Locate every blood parasite and identify its species.
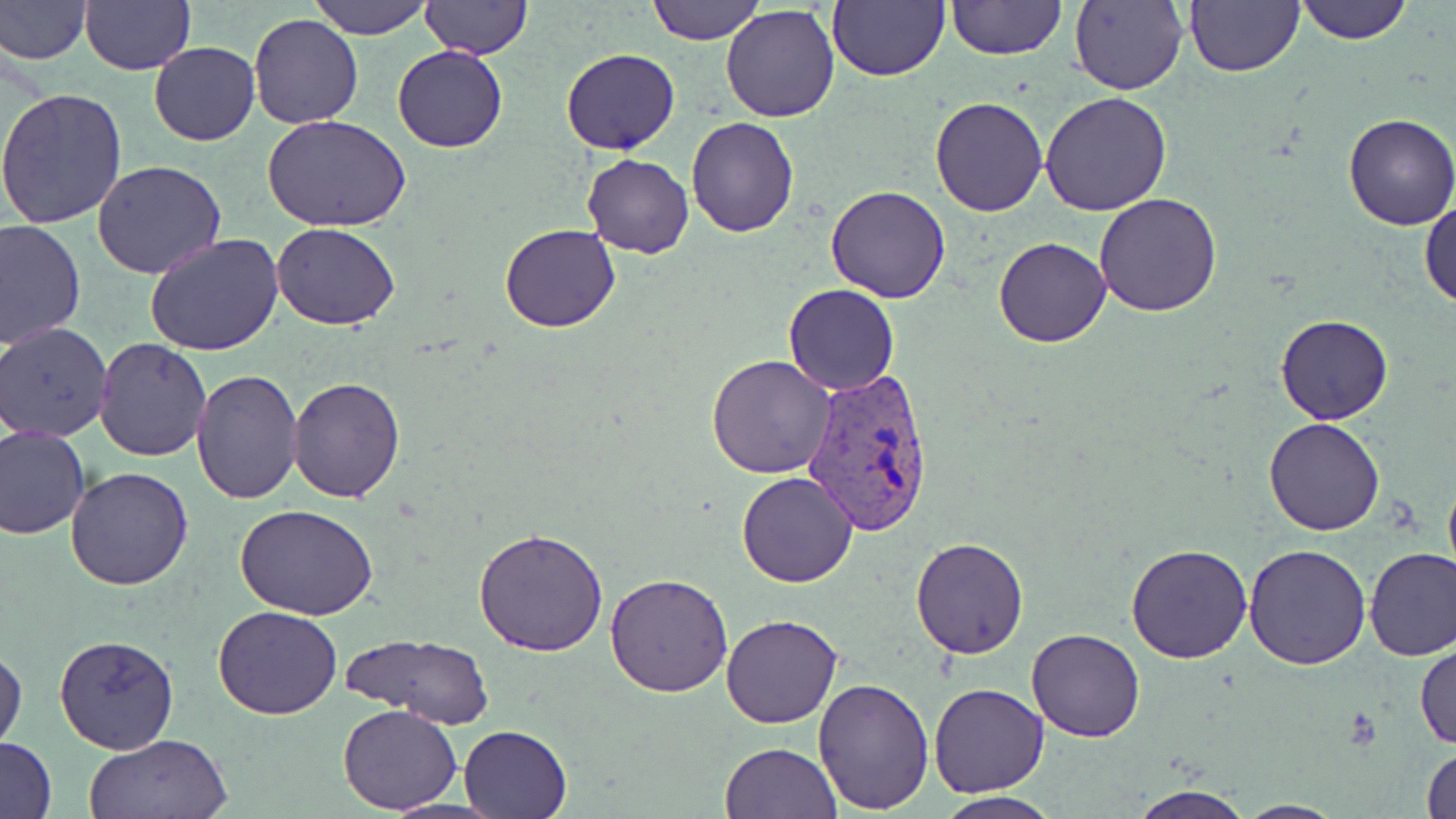

Approximate bounding boxes as named x1/y1/x2/y2 corners in pixels.
Plasmodium vivax-infected red blood cells: (x1=798, y1=365, x2=938, y2=537).
No Plasmodium falciparum, Plasmodium ovale, Plasmodium malariae, Babesia divergens, or Trypanosoma brucei observed.

Summary:
  - Uninfected red blood cell locations: (x1=0, y1=0, x2=91, y2=66), (x1=80, y1=0, x2=195, y2=75), (x1=309, y1=0, x2=433, y2=40), (x1=422, y1=0, x2=529, y2=59), (x1=647, y1=0, x2=763, y2=44), (x1=826, y1=0, x2=948, y2=83), (x1=947, y1=0, x2=1065, y2=61), (x1=1184, y1=0, x2=1305, y2=76), (x1=1294, y1=0, x2=1415, y2=45), (x1=1069, y1=1, x2=1187, y2=94), (x1=720, y1=3, x2=840, y2=123), (x1=250, y1=13, x2=363, y2=129), (x1=148, y1=41, x2=261, y2=146), (x1=392, y1=44, x2=507, y2=153), (x1=560, y1=48, x2=679, y2=156), (x1=0, y1=89, x2=129, y2=231), (x1=1040, y1=92, x2=1172, y2=214), (x1=930, y1=97, x2=1048, y2=217), (x1=1342, y1=111, x2=1456, y2=231), (x1=263, y1=114, x2=410, y2=234), (x1=685, y1=118, x2=800, y2=237), (x1=581, y1=152, x2=694, y2=258), (x1=92, y1=162, x2=226, y2=281), (x1=825, y1=184, x2=951, y2=303), (x1=1094, y1=193, x2=1222, y2=318), (x1=1420, y1=197, x2=1456, y2=310), (x1=0, y1=218, x2=86, y2=349), (x1=272, y1=223, x2=401, y2=330), (x1=499, y1=223, x2=622, y2=332), (x1=144, y1=234, x2=284, y2=356), (x1=992, y1=237, x2=1110, y2=349), (x1=783, y1=284, x2=899, y2=396), (x1=1275, y1=313, x2=1392, y2=424), (x1=1, y1=322, x2=115, y2=441), (x1=94, y1=339, x2=211, y2=461), (x1=707, y1=354, x2=838, y2=478), (x1=191, y1=368, x2=302, y2=504), (x1=288, y1=376, x2=406, y2=502), (x1=1265, y1=417, x2=1384, y2=535), (x1=0, y1=425, x2=91, y2=538), (x1=65, y1=466, x2=195, y2=590), (x1=1441, y1=469, x2=1456, y2=593), (x1=735, y1=472, x2=858, y2=588), (x1=238, y1=505, x2=378, y2=621), (x1=473, y1=528, x2=607, y2=656), (x1=909, y1=536, x2=1031, y2=658), (x1=1125, y1=542, x2=1254, y2=663), (x1=1242, y1=542, x2=1372, y2=669), (x1=1364, y1=546, x2=1456, y2=661), (x1=604, y1=572, x2=732, y2=696), (x1=213, y1=604, x2=341, y2=720), (x1=721, y1=613, x2=845, y2=729), (x1=1025, y1=629, x2=1146, y2=743), (x1=54, y1=635, x2=180, y2=754), (x1=345, y1=635, x2=495, y2=730), (x1=1415, y1=639, x2=1456, y2=751), (x1=1, y1=642, x2=26, y2=753), (x1=812, y1=675, x2=935, y2=813), (x1=930, y1=683, x2=1049, y2=799), (x1=337, y1=704, x2=464, y2=814), (x1=458, y1=723, x2=572, y2=818), (x1=83, y1=733, x2=232, y2=818), (x1=1, y1=736, x2=57, y2=817), (x1=719, y1=742, x2=840, y2=819), (x1=1421, y1=743, x2=1456, y2=819), (x1=1125, y1=784, x2=1254, y2=819), (x1=933, y1=792, x2=1062, y2=819), (x1=1232, y1=799, x2=1347, y2=818)
  - Slide-level diagnosis: Plasmodium vivax
  - Stain: May-Grünwald-Giemsa
  - Magnification: 1000x
  - Preparation: thin blood film
  - Field of view: single
  - Modality: light microscopy
  - Image size: 1456×819 pixels